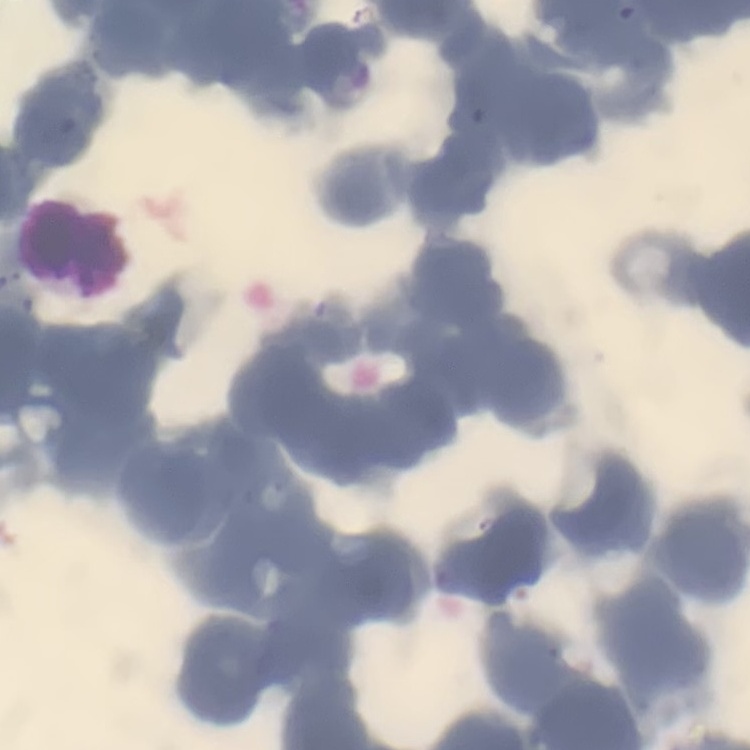 The erythrocytes exhibit rouleaux formation. Field's or Giemsa stain. Thin blood film. One tile cut from a larger photomicrograph.